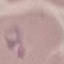

Summary:
  - Malaria status: parasitized
  - Stain: Giemsa
  - Capture: smartphone through the microscope eyepiece
  - Image type: cell patch, automatically extracted from a larger field of view and resized to 64 × 64 pixels
  - Preparation: thin blood film